Classify this cell by malaria status.
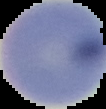
It is uninfected.

Image is 106×109 pixels. Segmented cell region on a black background. From a thin blood smear.